State the blood parasite species.
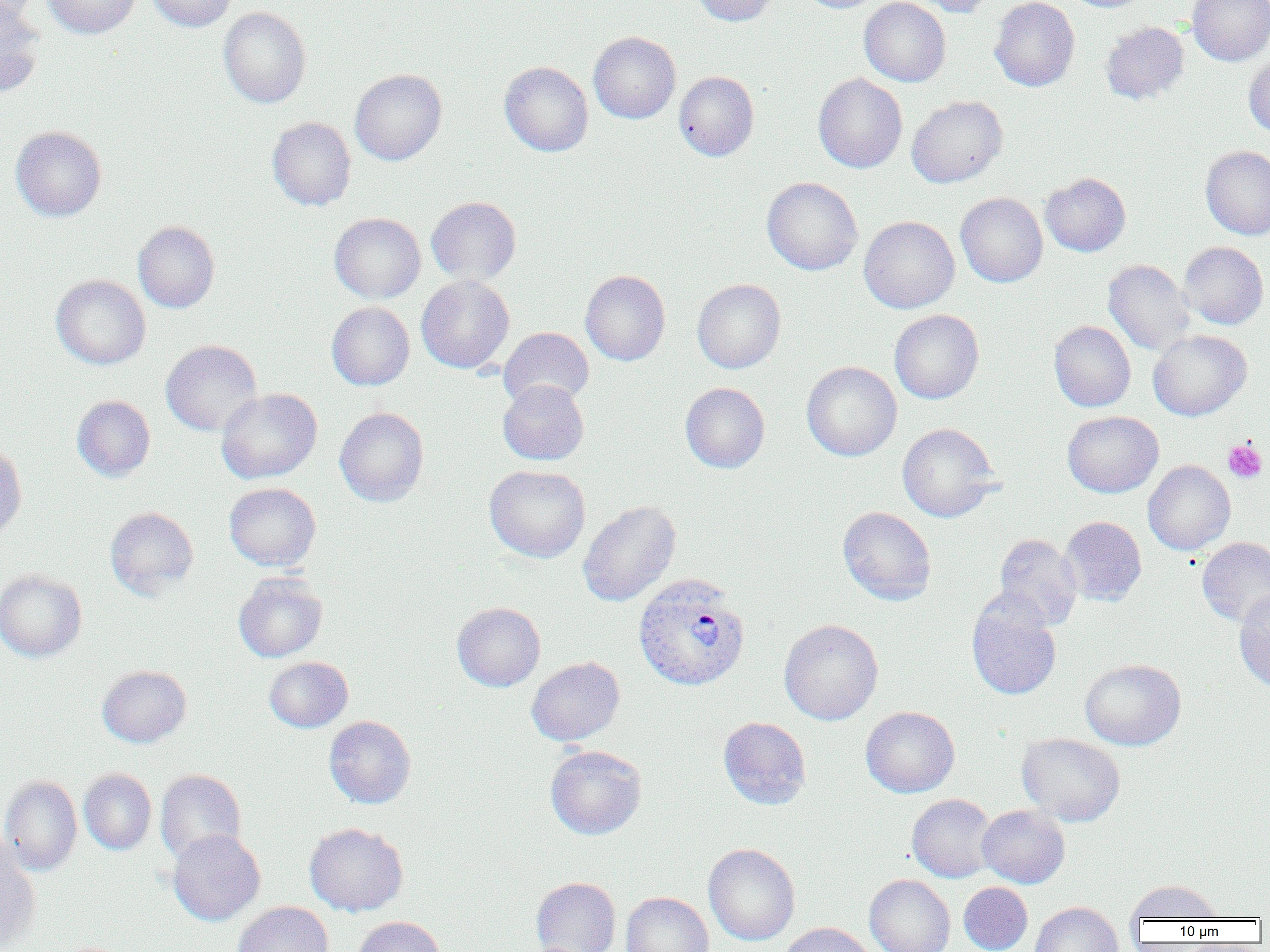
Plasmodium vivax.

Summary:
  - Coordinate format: approximate bounding boxes as [x1, y1, x2, y2] in pixels
  - Plasmodium vivax-infected red blood cell locations: [633, 573, 751, 691]
  - Platelet locations: [1223, 440, 1267, 483]
  - Uninfected red blood cell locations: [0, 0, 42, 25], [43, 0, 140, 39], [146, 0, 238, 32], [692, 0, 779, 26], [796, 0, 885, 13], [859, 0, 950, 87], [907, 0, 996, 17], [990, 0, 1079, 91], [1061, 0, 1151, 13], [1186, 0, 1270, 65], [0, 1, 45, 98], [218, 7, 311, 107], [1100, 22, 1189, 104], [588, 32, 680, 123], [1244, 52, 1270, 138], [499, 61, 593, 156], [349, 68, 447, 165], [674, 71, 759, 161], [813, 74, 907, 173], [907, 95, 1008, 188], [267, 117, 356, 211], [11, 126, 106, 221], [1200, 145, 1270, 240], [1040, 173, 1131, 257], [761, 177, 863, 275], [955, 193, 1047, 287], [426, 196, 521, 286], [329, 213, 426, 303], [859, 216, 960, 314], [133, 221, 220, 312], [1178, 241, 1269, 330], [1103, 259, 1195, 356], [580, 270, 670, 365], [51, 274, 151, 369], [416, 275, 514, 373], [692, 279, 786, 373], [326, 301, 414, 390], [889, 309, 984, 404], [1049, 321, 1135, 411], [498, 327, 594, 410], [1148, 330, 1252, 421], [161, 340, 263, 436], [802, 362, 901, 461], [498, 380, 589, 465], [680, 382, 770, 473], [216, 388, 322, 484], [71, 395, 155, 481], [334, 407, 429, 507], [1062, 411, 1163, 497], [897, 423, 1000, 522], [0, 442, 27, 545], [1143, 460, 1235, 555], [484, 465, 590, 562], [224, 483, 321, 571], [578, 500, 680, 607], [105, 507, 199, 598], [838, 507, 936, 605], [1059, 516, 1146, 606], [993, 534, 1082, 630], [1196, 537, 1270, 626], [0, 569, 87, 662], [233, 573, 328, 662], [1234, 590, 1270, 693], [967, 597, 1061, 700], [452, 602, 545, 691], [779, 619, 883, 725], [264, 656, 353, 732], [526, 657, 625, 746], [1080, 658, 1186, 750], [97, 665, 191, 747], [861, 706, 960, 797], [324, 716, 416, 809], [718, 716, 811, 809], [1017, 732, 1125, 826], [545, 745, 647, 839], [78, 768, 156, 855], [155, 769, 246, 864], [0, 775, 82, 875], [907, 794, 997, 883], [977, 805, 1070, 888], [305, 822, 408, 916], [167, 829, 265, 925], [0, 840, 42, 950], [703, 843, 800, 945], [864, 874, 955, 952], [531, 877, 621, 952], [1124, 880, 1224, 922], [958, 882, 1032, 952], [621, 892, 714, 952], [233, 901, 333, 952], [1030, 901, 1123, 952], [352, 916, 445, 952], [778, 922, 876, 952]
  - Field of view: single
  - Magnification: 1000x
  - Preparation: thin blood smear
  - Image size: 1270×952 pixels
  - Modality: light microscopy